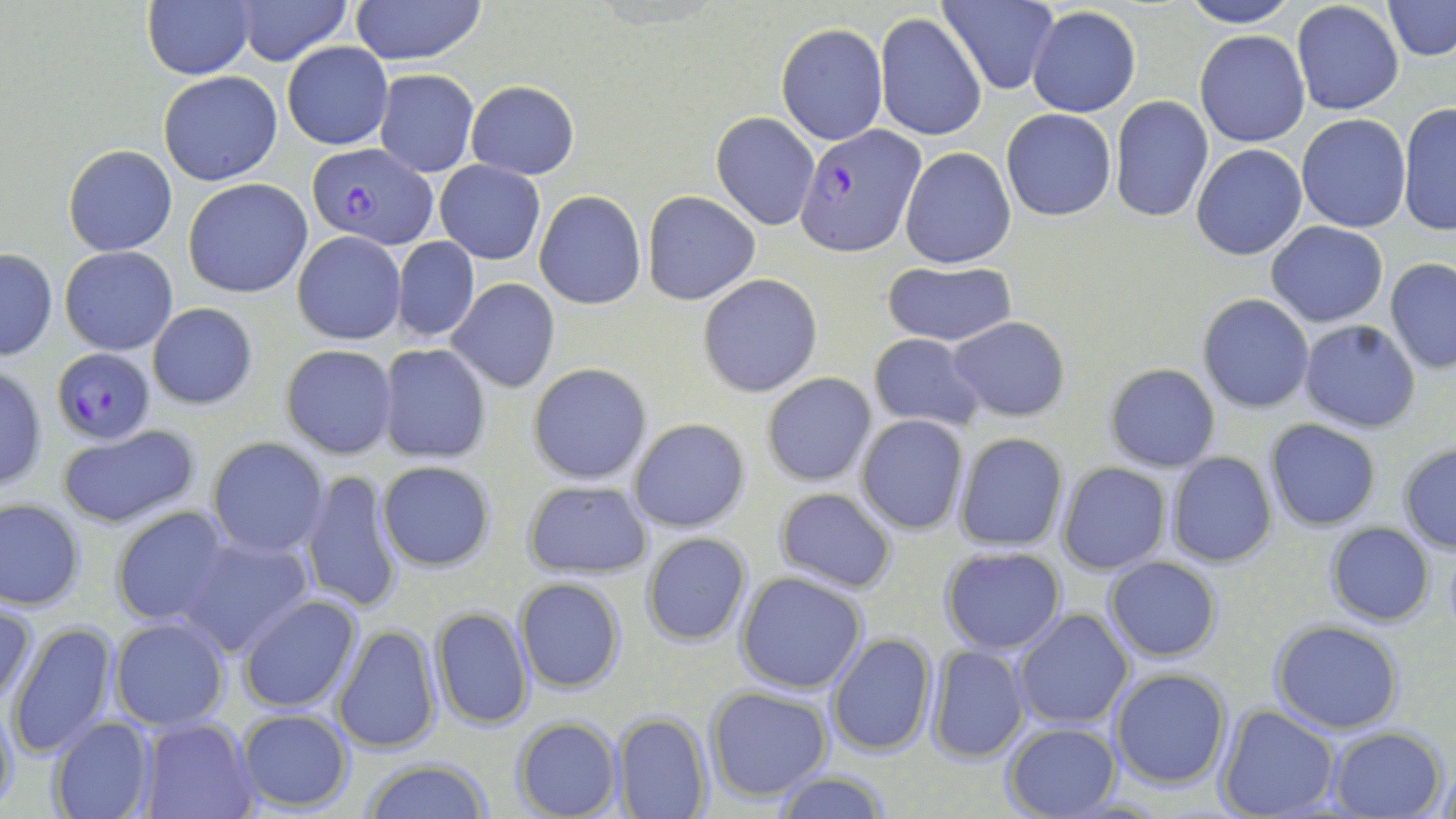

Summary:
  - Coordinate format: approximate bounding boxes as [x1, y1, x2, y2] in pixels
  - Plasmodium falciparum-infected red blood cell locations: [796, 126, 922, 253], [308, 141, 438, 247], [52, 348, 154, 444]
  - Uninfected red blood cell locations: [232, 0, 351, 64], [351, 0, 487, 66], [938, 0, 1059, 93], [1177, 0, 1300, 28], [1383, 0, 1455, 60], [1291, 1, 1404, 117], [143, 2, 254, 79], [1313, 4, 1455, 78], [1025, 6, 1140, 117], [876, 13, 986, 140], [776, 23, 886, 144], [1193, 28, 1310, 146], [281, 41, 392, 150], [374, 69, 478, 176], [158, 71, 283, 187], [465, 80, 580, 179], [1109, 96, 1212, 221], [1397, 101, 1456, 238], [1001, 108, 1117, 222], [710, 111, 820, 231], [1297, 115, 1411, 232], [62, 142, 178, 256], [1191, 143, 1307, 261], [899, 147, 1016, 269], [435, 159, 545, 264], [183, 178, 313, 298], [534, 190, 646, 310], [642, 190, 759, 305], [1266, 221, 1389, 327], [292, 230, 406, 345], [393, 237, 479, 343], [60, 246, 178, 354], [0, 249, 57, 361], [1385, 257, 1456, 375], [879, 260, 1018, 347], [696, 273, 822, 397], [448, 279, 560, 392], [1198, 293, 1315, 414], [148, 303, 258, 409], [948, 317, 1071, 422], [1298, 321, 1422, 433], [868, 332, 986, 430], [377, 343, 491, 464], [280, 344, 398, 459], [527, 362, 652, 486], [1104, 363, 1221, 473], [0, 365, 47, 493], [762, 372, 877, 488], [856, 415, 970, 535], [627, 418, 751, 535], [1264, 419, 1381, 530], [57, 425, 200, 530], [953, 433, 1068, 553], [207, 436, 329, 557], [1398, 443, 1456, 553], [1166, 453, 1278, 568], [376, 461, 499, 572], [1056, 462, 1172, 574], [300, 467, 409, 618], [521, 478, 652, 580], [773, 487, 898, 594], [1, 498, 86, 610], [110, 506, 234, 630], [1325, 522, 1435, 626], [178, 532, 315, 657], [640, 532, 752, 646], [940, 546, 1067, 654], [1103, 555, 1222, 662], [735, 571, 868, 694], [514, 577, 626, 694], [236, 594, 363, 714], [0, 597, 39, 710], [432, 605, 533, 730], [1013, 608, 1134, 730], [109, 617, 231, 731], [1270, 621, 1404, 734], [7, 622, 119, 759], [333, 623, 442, 756], [826, 633, 937, 757], [926, 645, 1030, 764], [1109, 668, 1230, 789], [705, 686, 834, 802], [0, 693, 20, 816], [1215, 706, 1340, 818], [235, 708, 354, 813], [613, 711, 712, 818], [48, 717, 157, 819], [142, 717, 261, 819], [511, 717, 624, 819], [1002, 722, 1121, 817], [1325, 726, 1447, 819], [359, 760, 496, 818], [1436, 764, 1455, 819], [773, 769, 891, 819]
  - Slide-level diagnosis: Plasmodium falciparum
  - Preparation: thin blood film
  - Magnification: 1000x
  - Stain: May-Grünwald-Giemsa
  - Modality: optical microscopy
  - Field of view: one of a larger specimen
  - Image size: 1456×819 pixels